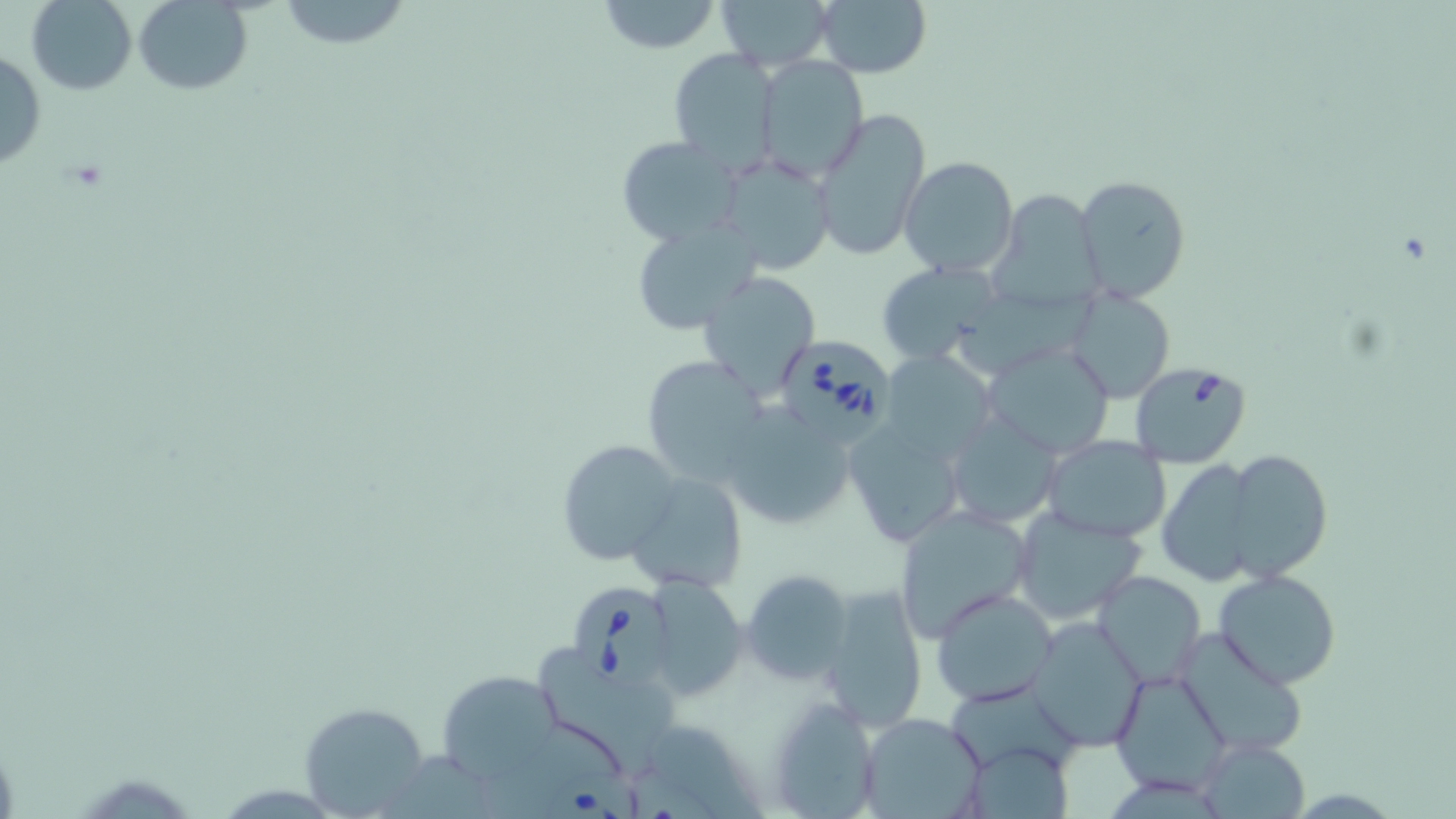
Summary:
  - Coordinate format: approximate bounding boxes as (x1, y1, x2, y2) in pixels
  - Uninfected red blood cell locations: (26, 0, 138, 94), (279, 0, 414, 48), (594, 0, 722, 53), (715, 0, 834, 70), (811, 0, 932, 79), (133, 1, 254, 94), (668, 48, 780, 176), (0, 49, 46, 171), (756, 57, 869, 180), (812, 105, 931, 262), (615, 136, 744, 247), (715, 154, 837, 275), (899, 157, 1020, 278), (1077, 176, 1191, 302), (988, 189, 1102, 313), (627, 218, 766, 337), (878, 262, 1000, 364), (697, 271, 821, 398), (963, 289, 1090, 375), (1068, 289, 1175, 403), (981, 339, 1116, 459), (881, 352, 997, 465), (639, 357, 773, 487), (723, 407, 853, 532), (946, 413, 1064, 529), (842, 418, 967, 550), (1042, 436, 1171, 542), (556, 437, 683, 566), (1223, 450, 1333, 580), (1157, 457, 1259, 587), (624, 473, 747, 593), (894, 505, 1033, 642), (1013, 506, 1146, 623), (1212, 567, 1342, 689), (740, 569, 853, 686), (1091, 569, 1207, 688), (647, 579, 748, 697), (820, 580, 930, 730), (932, 588, 1059, 709), (1028, 616, 1147, 748), (1173, 625, 1310, 759), (542, 653, 681, 770), (436, 669, 559, 782), (1111, 669, 1233, 796), (766, 695, 885, 816), (300, 702, 432, 817), (860, 712, 986, 818), (959, 740, 1076, 817), (1196, 740, 1310, 818)
  - Babesia divergens-infected red blood cell locations: (772, 334, 898, 443), (1129, 361, 1252, 468), (572, 583, 679, 693), (543, 766, 641, 819)
  - Slide-level diagnosis: Babesia divergens
  - Stain: May-Grünwald-Giemsa
  - Modality: optical microscopy
  - Field of view: one of a larger specimen
  - Image size: 1456×819 pixels
  - Magnification: 1000x
  - Preparation: thin blood smear